Identify the parasite.
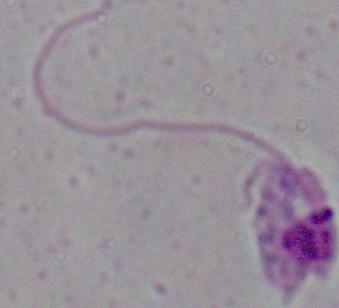
Leishmania.

modality: photomicrograph
magnification: 1000x